Outline each Plasmodium malariae-infected red blood cell.
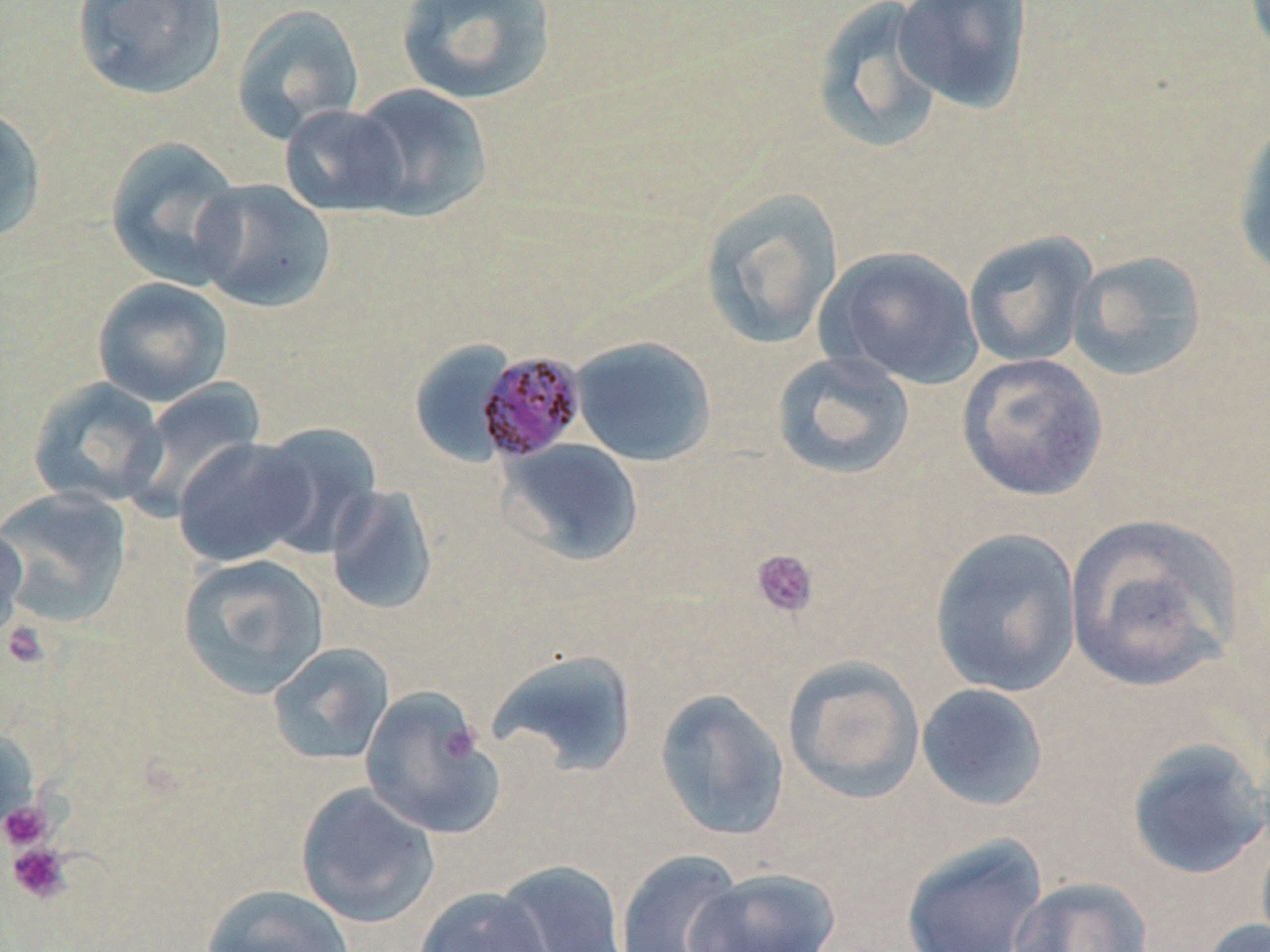
Approximate bounding boxes as (x1, y1, x2, y2) in pixels.
Plasmodium malariae-infected red blood cells: (477, 349, 588, 462).

{
  "slide_level_diagnosis": "Plasmodium malariae",
  "stain": "May-Grünwald-Giemsa",
  "platelet_locations": "approximate bounding boxes as (x1, y1, x2, y2) in pixels: (751, 549, 819, 618), (1, 621, 49, 670), (441, 723, 482, 764), (0, 800, 55, 851), (7, 842, 73, 904)",
  "uninfected_red_blood_cell_locations": "approximate bounding boxes as (x1, y1, x2, y2) in pixels: (70, 0, 229, 102), (395, 0, 557, 106), (893, 0, 1034, 115), (809, 1, 948, 153), (230, 4, 365, 143), (349, 83, 494, 222), (278, 104, 409, 218), (0, 106, 47, 245), (1232, 114, 1270, 282), (104, 136, 247, 290), (191, 178, 337, 314), (700, 188, 844, 350), (963, 231, 1098, 368), (819, 246, 984, 389), (1066, 249, 1209, 382), (91, 277, 234, 407), (571, 336, 717, 467), (407, 339, 517, 466), (771, 350, 916, 481), (956, 353, 1109, 501), (27, 377, 168, 510), (123, 378, 266, 520), (251, 422, 383, 558), (172, 437, 313, 567), (500, 438, 644, 566), (325, 485, 438, 617), (0, 486, 133, 629), (1064, 513, 1243, 694), (0, 521, 29, 645), (929, 527, 1082, 698), (177, 553, 329, 699), (267, 642, 395, 766), (485, 649, 641, 778), (782, 655, 925, 804), (916, 683, 1050, 812), (358, 686, 505, 839), (654, 688, 790, 842), (0, 726, 39, 841), (1125, 737, 1270, 880), (295, 783, 440, 929), (900, 833, 1049, 952), (614, 849, 745, 952), (493, 859, 630, 952), (687, 867, 840, 952), (1006, 876, 1153, 952), (200, 884, 355, 952), (413, 886, 554, 952), (1198, 917, 1270, 952)",
  "field_of_view": "one of a larger specimen",
  "magnification": "1000x",
  "preparation": "thin blood film",
  "image_size": "1270×952 pixels",
  "modality": "light microscopy"
}